Assess for malaria.
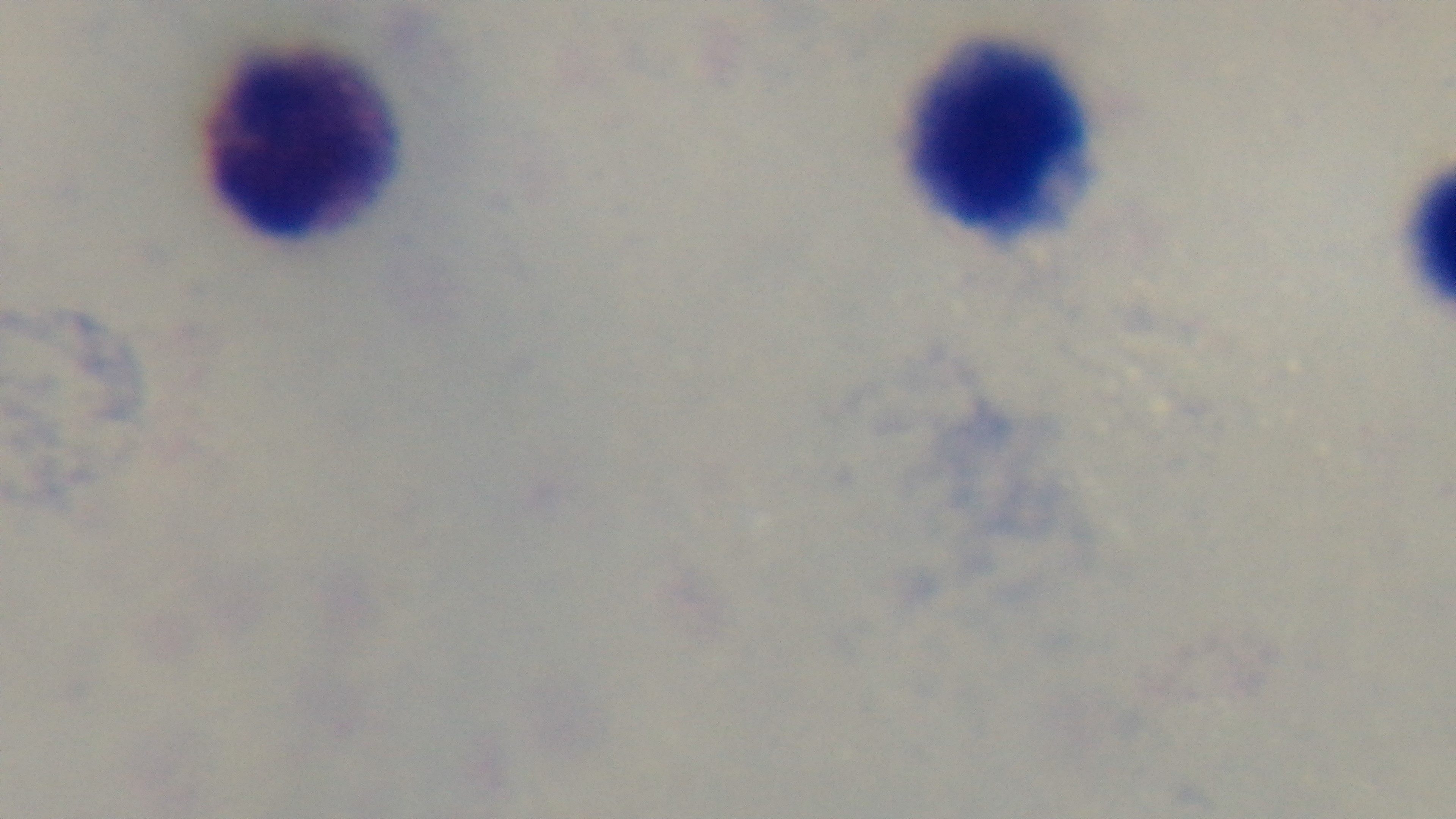

Uninfected.

field of view = one from the slide
objective = 100x oil immersion
capture = mounted 4K digital camera
preparation = thick blood film
stain = Giemsa
modality = light microscopy